Locate every uninfected red blood cell.
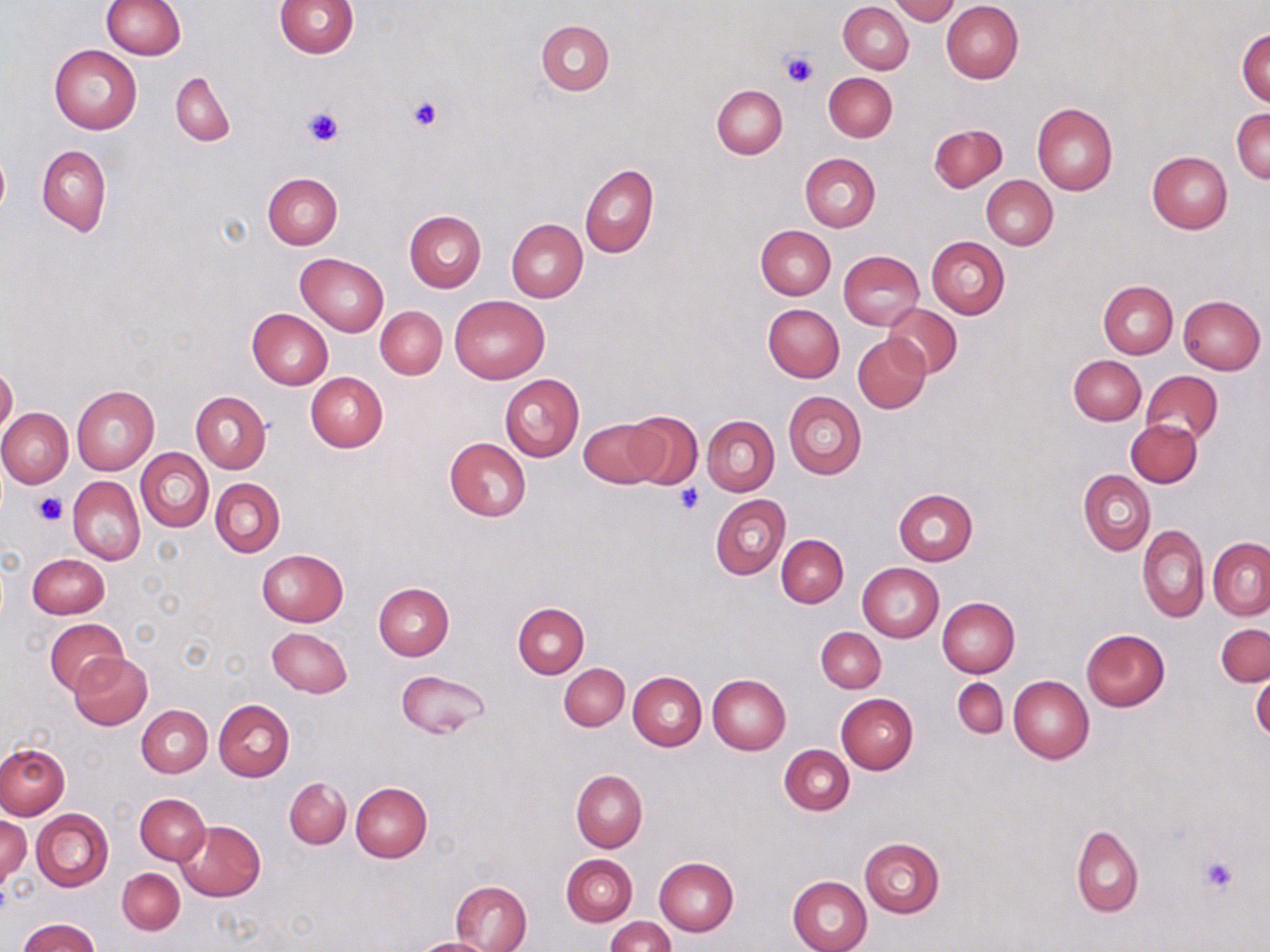

Approximate bounding boxes as named x1/y1/x2/y2 corners in pixels.
Uninfected red blood cells: (x1=101, y1=0, x2=186, y2=59), (x1=274, y1=0, x2=357, y2=57), (x1=890, y1=0, x2=960, y2=24), (x1=941, y1=1, x2=1024, y2=84), (x1=839, y1=2, x2=914, y2=74), (x1=536, y1=20, x2=615, y2=95), (x1=1237, y1=29, x2=1269, y2=107), (x1=49, y1=45, x2=142, y2=134), (x1=172, y1=70, x2=235, y2=146), (x1=824, y1=72, x2=897, y2=141), (x1=712, y1=85, x2=788, y2=158), (x1=1032, y1=103, x2=1117, y2=194), (x1=1231, y1=108, x2=1270, y2=184), (x1=930, y1=123, x2=1008, y2=191), (x1=0, y1=145, x2=9, y2=221), (x1=36, y1=145, x2=110, y2=235), (x1=1147, y1=151, x2=1233, y2=232), (x1=800, y1=153, x2=881, y2=231), (x1=580, y1=164, x2=658, y2=258), (x1=263, y1=173, x2=342, y2=249), (x1=981, y1=175, x2=1058, y2=249), (x1=405, y1=210, x2=487, y2=292), (x1=506, y1=217, x2=587, y2=302), (x1=756, y1=225, x2=835, y2=300), (x1=925, y1=236, x2=1010, y2=319), (x1=838, y1=250, x2=923, y2=328), (x1=295, y1=252, x2=389, y2=336), (x1=1099, y1=281, x2=1177, y2=359), (x1=448, y1=295, x2=549, y2=383), (x1=1178, y1=295, x2=1266, y2=374), (x1=763, y1=303, x2=845, y2=382), (x1=881, y1=303, x2=962, y2=378), (x1=375, y1=306, x2=447, y2=379), (x1=246, y1=309, x2=333, y2=390), (x1=853, y1=334, x2=931, y2=413), (x1=1069, y1=355, x2=1146, y2=425), (x1=0, y1=364, x2=18, y2=437), (x1=306, y1=371, x2=388, y2=452), (x1=1140, y1=371, x2=1222, y2=445), (x1=500, y1=373, x2=585, y2=461), (x1=72, y1=385, x2=159, y2=475), (x1=190, y1=391, x2=271, y2=474), (x1=782, y1=391, x2=867, y2=479), (x1=0, y1=408, x2=73, y2=488), (x1=624, y1=410, x2=702, y2=489), (x1=702, y1=415, x2=779, y2=495), (x1=578, y1=417, x2=663, y2=488), (x1=1126, y1=419, x2=1203, y2=487), (x1=444, y1=438, x2=531, y2=521), (x1=136, y1=448, x2=213, y2=532), (x1=1078, y1=470, x2=1155, y2=555), (x1=68, y1=477, x2=145, y2=565), (x1=211, y1=478, x2=286, y2=556), (x1=892, y1=490, x2=977, y2=566), (x1=710, y1=495, x2=790, y2=579), (x1=1138, y1=525, x2=1209, y2=622), (x1=777, y1=534, x2=849, y2=607), (x1=1208, y1=538, x2=1270, y2=619), (x1=257, y1=549, x2=348, y2=626), (x1=28, y1=554, x2=109, y2=618), (x1=858, y1=563, x2=944, y2=642), (x1=374, y1=584, x2=454, y2=660), (x1=938, y1=598, x2=1020, y2=678), (x1=513, y1=602, x2=589, y2=677), (x1=45, y1=618, x2=127, y2=694), (x1=1216, y1=623, x2=1270, y2=687), (x1=266, y1=627, x2=353, y2=697), (x1=816, y1=627, x2=886, y2=693), (x1=1082, y1=629, x2=1170, y2=711), (x1=69, y1=653, x2=153, y2=731), (x1=559, y1=663, x2=630, y2=730), (x1=397, y1=669, x2=490, y2=738), (x1=629, y1=672, x2=706, y2=751), (x1=708, y1=673, x2=791, y2=754), (x1=1251, y1=673, x2=1270, y2=741), (x1=1009, y1=676, x2=1094, y2=763), (x1=953, y1=678, x2=1007, y2=739), (x1=836, y1=693, x2=917, y2=775), (x1=213, y1=699, x2=295, y2=783), (x1=137, y1=704, x2=212, y2=777), (x1=0, y1=744, x2=69, y2=820), (x1=780, y1=745, x2=854, y2=815), (x1=571, y1=770, x2=647, y2=852), (x1=285, y1=778, x2=351, y2=848), (x1=351, y1=782, x2=432, y2=861), (x1=135, y1=793, x2=209, y2=865), (x1=135, y1=801, x2=253, y2=889), (x1=31, y1=809, x2=114, y2=891), (x1=1, y1=815, x2=30, y2=890), (x1=176, y1=820, x2=264, y2=901), (x1=1070, y1=826, x2=1144, y2=918), (x1=859, y1=838, x2=943, y2=918), (x1=561, y1=854, x2=637, y2=926), (x1=654, y1=857, x2=738, y2=936), (x1=117, y1=868, x2=185, y2=934), (x1=788, y1=876, x2=872, y2=952), (x1=450, y1=880, x2=533, y2=952), (x1=605, y1=916, x2=674, y2=952), (x1=17, y1=918, x2=100, y2=952), (x1=412, y1=938, x2=500, y2=952).

slide-level diagnosis = no evidence of blood parasites
magnification = 1000x
modality = light microscopy
platelet locations = approximate bounding boxes as named x1/y1/x2/y2 corners in pixels: (x1=779, y1=48, x2=817, y2=88), (x1=408, y1=95, x2=443, y2=131), (x1=302, y1=106, x2=343, y2=148), (x1=676, y1=485, x2=704, y2=514), (x1=34, y1=492, x2=68, y2=526), (x1=1199, y1=854, x2=1239, y2=894)
preparation = thin blood film
stain = May-Grünwald-Giemsa
field of view = one of a larger specimen
image size = 1270×952 pixels